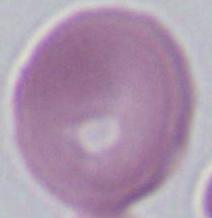 A red blood cell is shown. Micrograph. Captured at 1000x magnification.